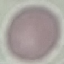

Summary:
  - Malaria status: uninfected
  - Stain: Giemsa
  - Image type: cell patch, automatically extracted from a larger field of view and resized to 64 × 64 pixels
  - Preparation: thin blood film
  - Capture: smartphone through the microscope eyepiece